Give the position of every malaria parasite.
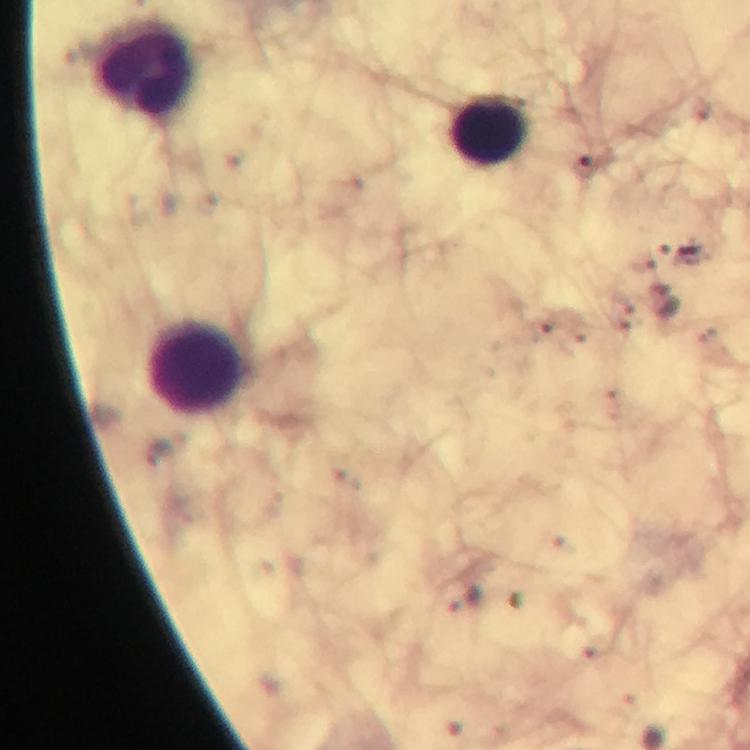

No malaria parasites seen.

Approximate centers as [x, y] in pixels. Leukocyte locations: [145, 70], [490, 131], [196, 370]. Image is 750×750 pixels. Photographed through the microscope with a smartphone camera. From a diagnostic examination for malaria. Thick blood film. 100x magnification. Immersion oil applied. Cropped region of a single field of view. Giemsa-stained preparation.